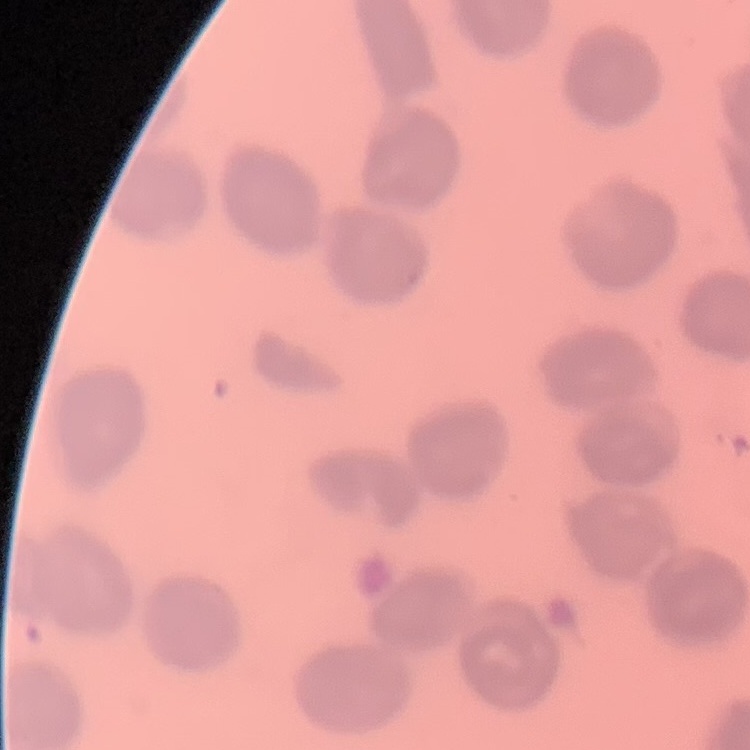 The red blood cells exhibit no rouleaux formation. Square crop of a larger photomicrograph. Field's or Giemsa stain. Thin blood smear.